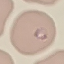
result = malaria parasites detected
stain = Giemsa
image type = automatically extracted cell patch, resized to 64 × 64 pixels
preparation = thin smear
capture = smartphone through the microscope eyepiece